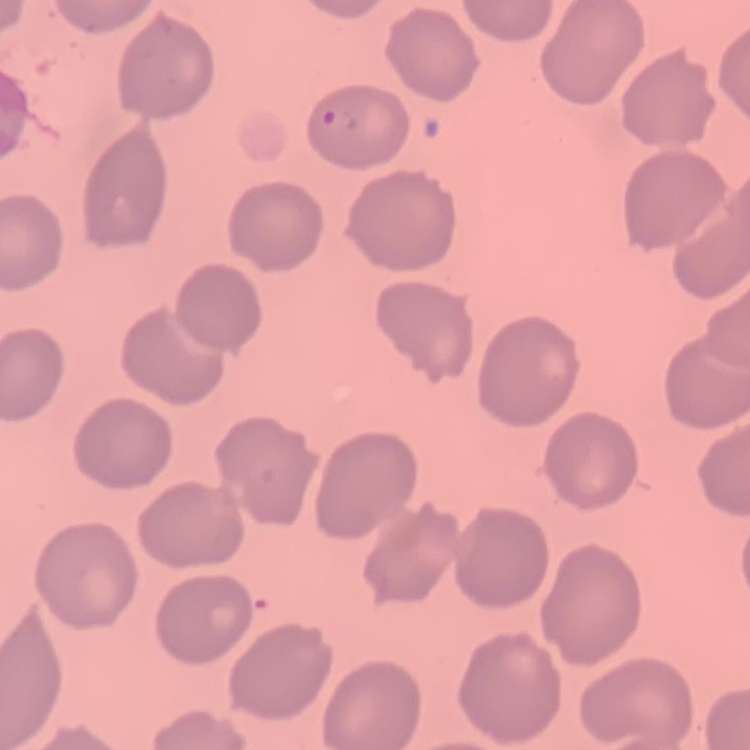

erythrocyte morphology = no rouleaux formation
stain = Field's or Giemsa
preparation = thin peripheral smear
image type = one tile cut from a larger photomicrograph